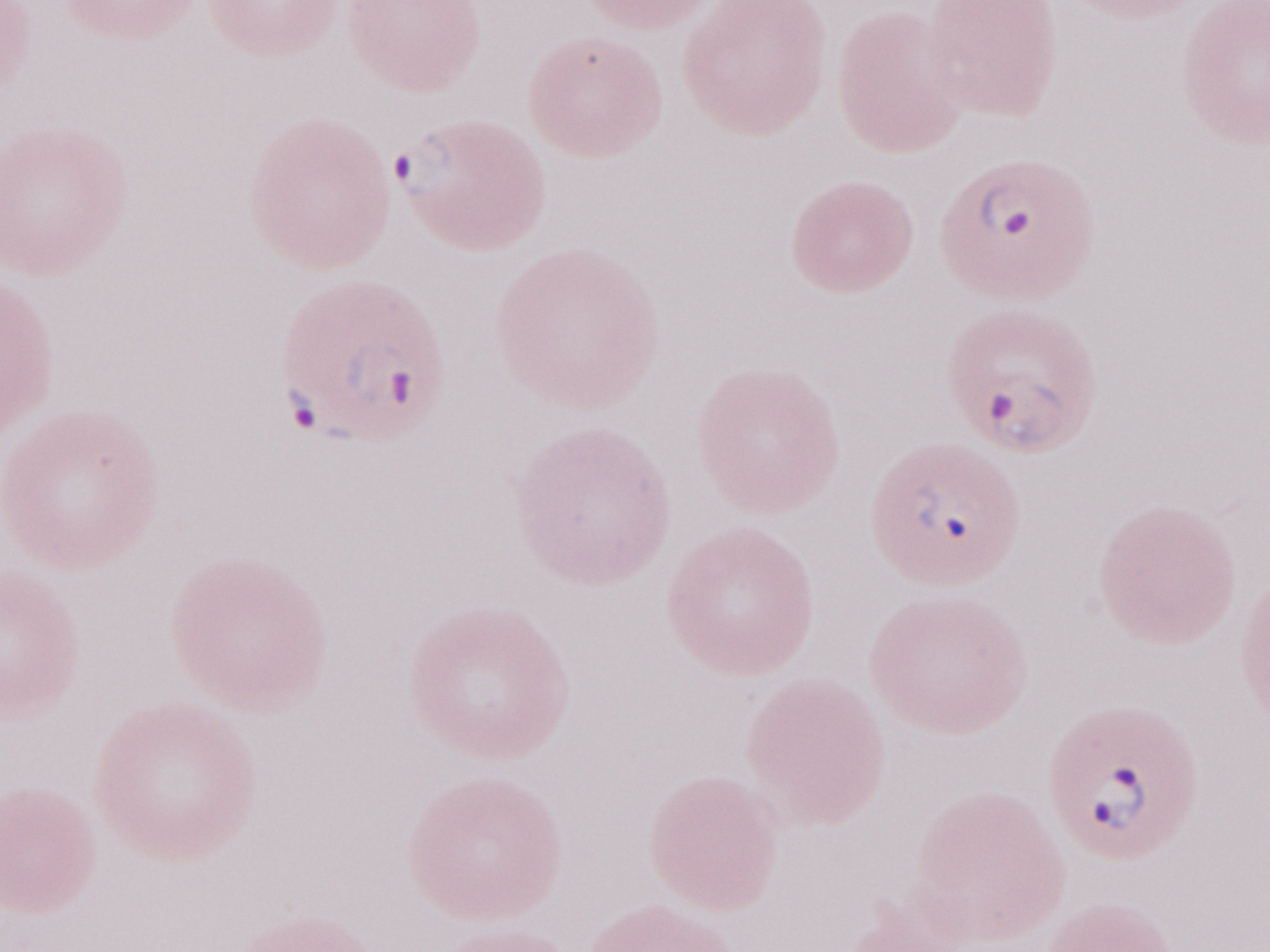
One field of this slide. Malaria diagnosis (patient-level): positive. Image is 1270×952 pixels. Thin blood smear. Olympus BX43 microscope, Olympus DP73 camera. May-Grünwald-Giemsa (MGG) stain. 1,000x magnification.